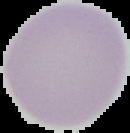

From a thin blood smear. Image is 130×133 pixels. Segmented cell region on a black background. Malaria status: uninfected.